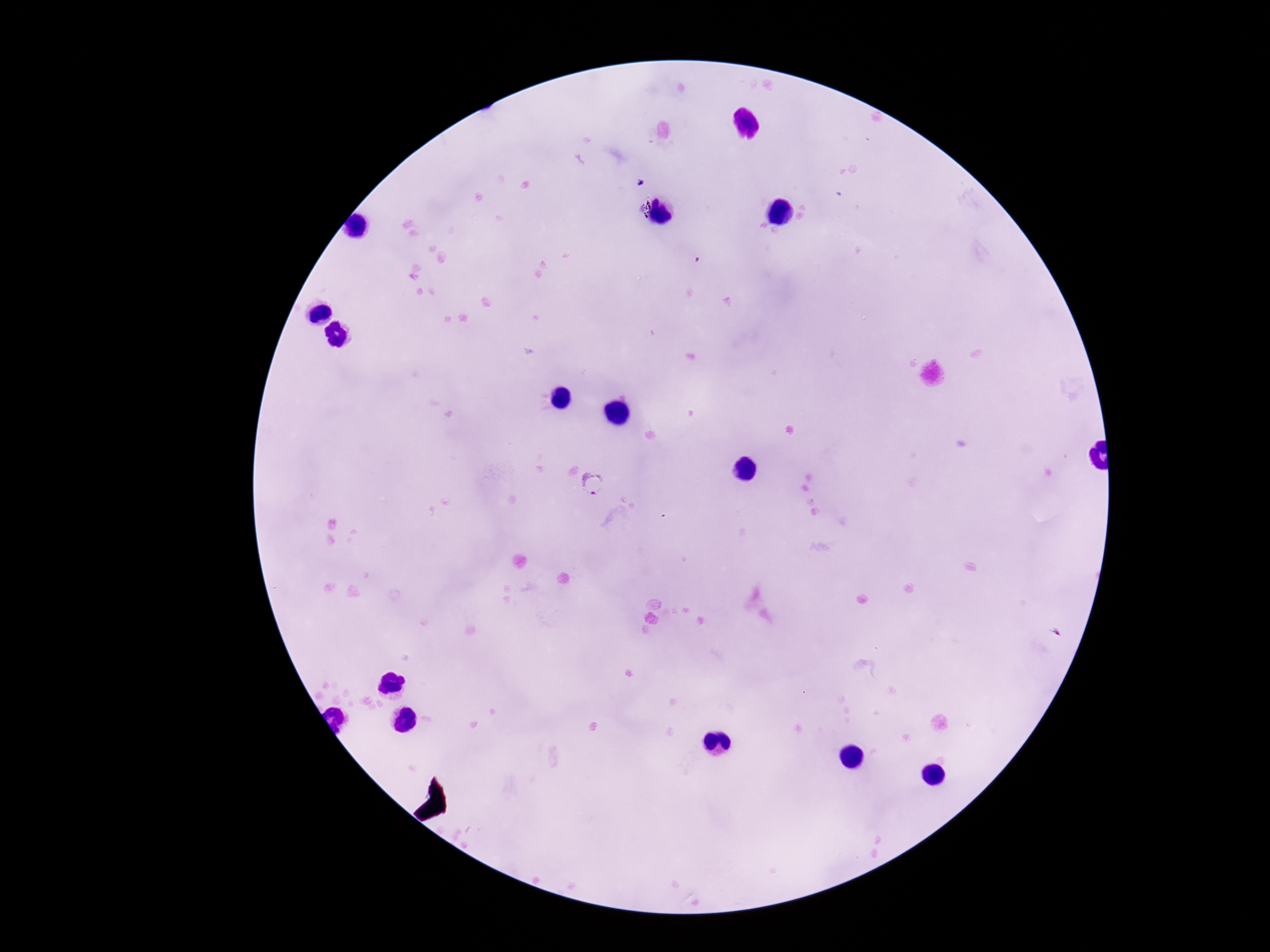 Approximate object centers, in pixels from the top-left corner. Plasmodium parasite locations: (x=641, y=183), (x=592, y=480). Smartphone photograph taken through the microscope eyepiece. 100x magnification. Thick blood film. Giemsa stain. One field from this slide. Patient malaria status: infected. Image is 1270×952 pixels.